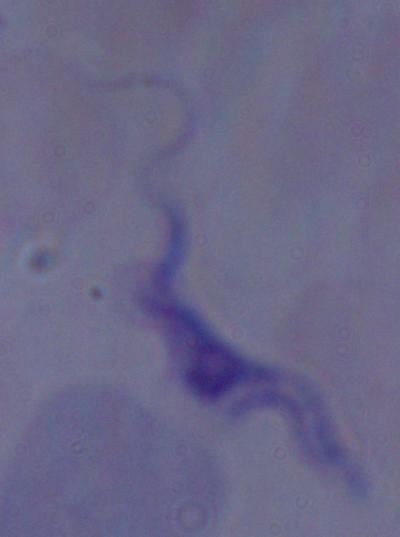

{
  "magnification": "1000x",
  "modality": "photomicrograph",
  "identification": "trypanosome"
}